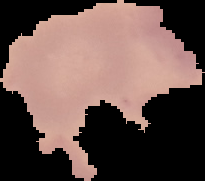

Segmented cell region on a black background. Malaria status: uninfected. Image is 205×181 pixels. From a thin blood smear.